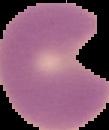

Image is 109×130 pixels. Result: malaria parasites identified. From a thin blood film. The area outside the segmented cell region is set to black.